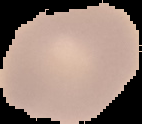

Summary:
  - Image size: 142×124 pixels
  - Malaria status: uninfected
  - Preparation: thin blood film
  - Image type: segmented cell region with the area outside set to black